Report the malaria status of this cell.
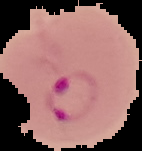
Parasitized.

From a thin blood smear. Image is 142×151 pixels. Cell region segmented out of the field of view; the surrounding area is masked to black.